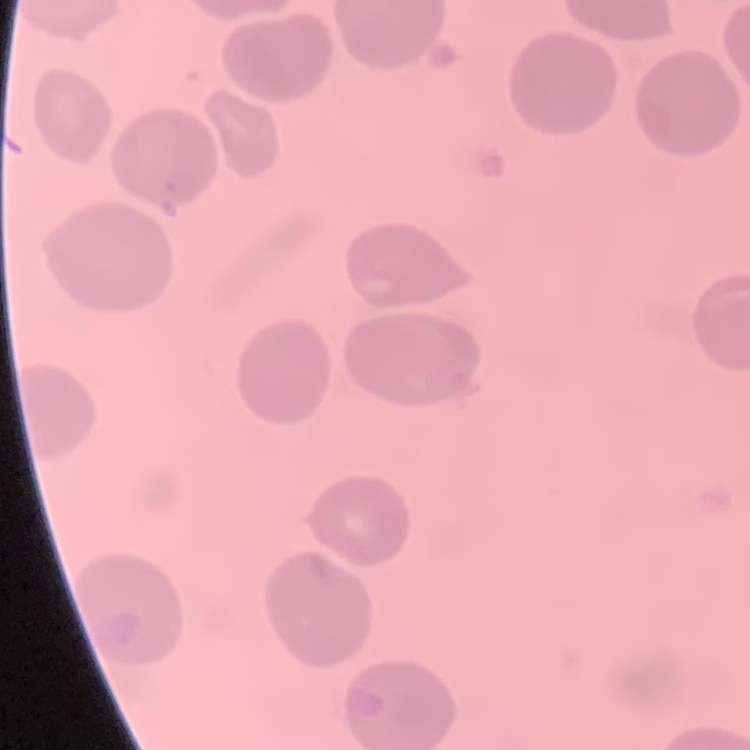
erythrocyte morphology = no rouleaux formation
image type = one tile cut from a larger photomicrograph
stain = Field's or Giemsa
preparation = thin blood film